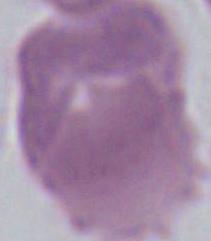

Summary:
  - Magnification: 1000x
  - Identification: red blood cell
  - Modality: micrograph